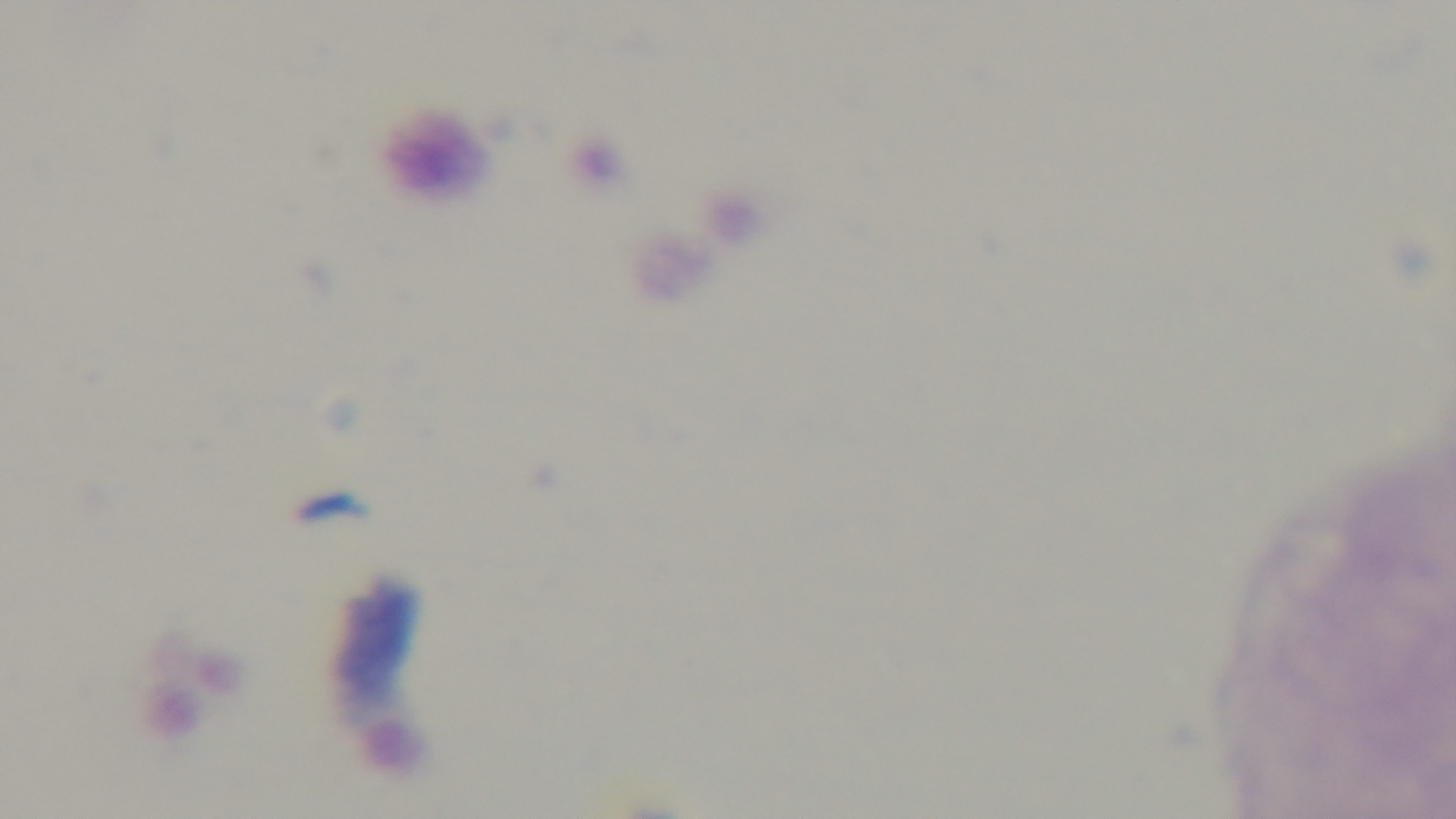
Summary:
  - Preparation: thick
  - Malaria status: uninfected
  - Field of view: one from the slide
  - Objective: 100x oil immersion
  - Modality: light microscopy
  - Capture: mounted 4K digital camera
  - Stain: Giemsa